Mark where leukocytes are.
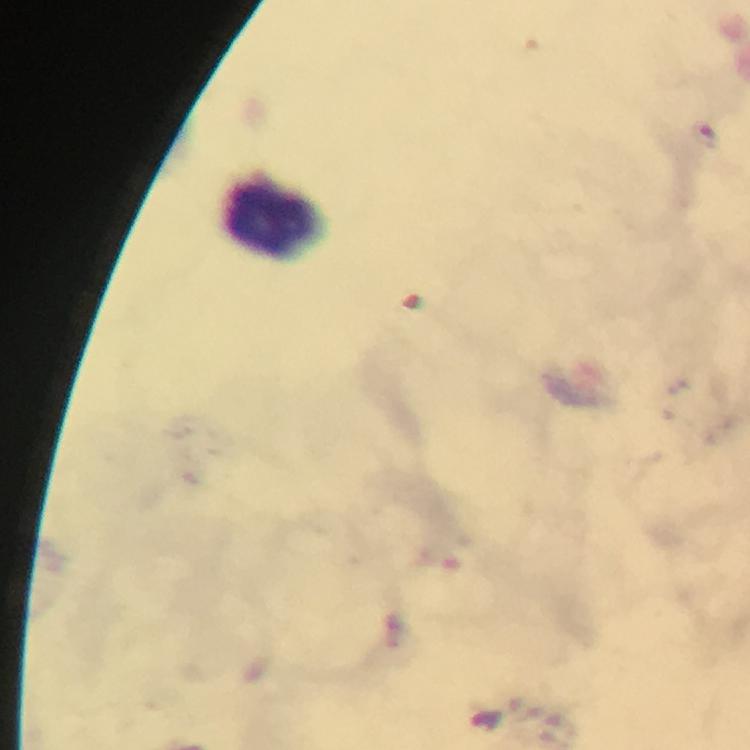

Approximate centers as (x, y) in pixels.
Leukocytes: (272, 217).

Malaria parasite locations: (711, 135). Immersion oil applied. A crop from one field of view. Image is 750×750 pixels. 100x magnification. Smartphone photograph taken through a microscope. From a malaria diagnostic workup. Thick smear. Giemsa-stained preparation.